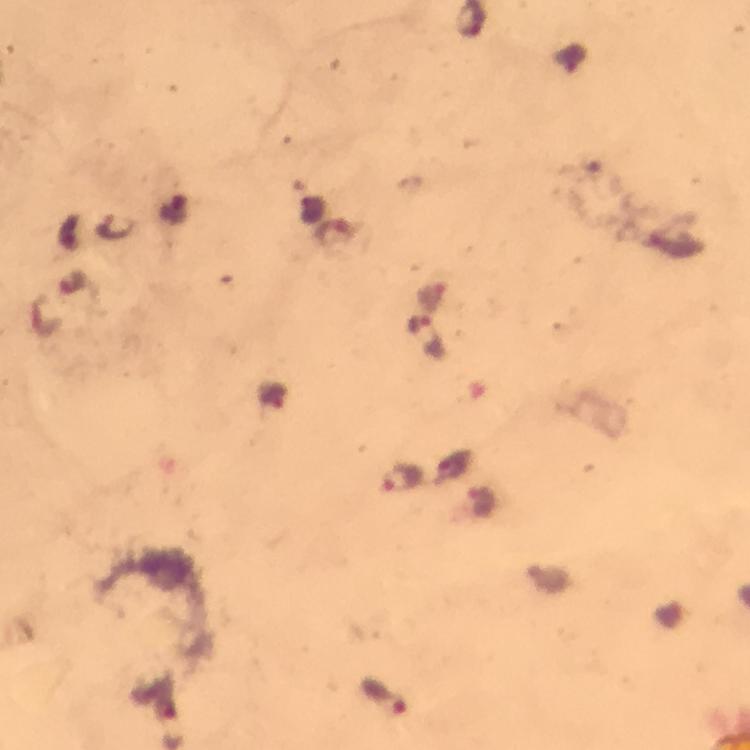
{
  "stain": "Giemsa",
  "magnification": "100x",
  "plasmodium_parasite_locations": "approximate centers as (x, y) in pixels: (116, 224), (403, 476), (382, 697)",
  "context": "from a diagnostic examination for malaria",
  "preparation": "thick blood film",
  "immersion_oil": "used",
  "cropped_from": "one field of view",
  "capture": "smartphone photograph through a microscope",
  "image_size": "750×750 pixels"
}